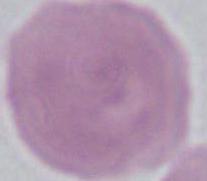
modality = photomicrograph
magnification = 1000x
identification = erythrocyte